Point out each Plasmodium parasite.
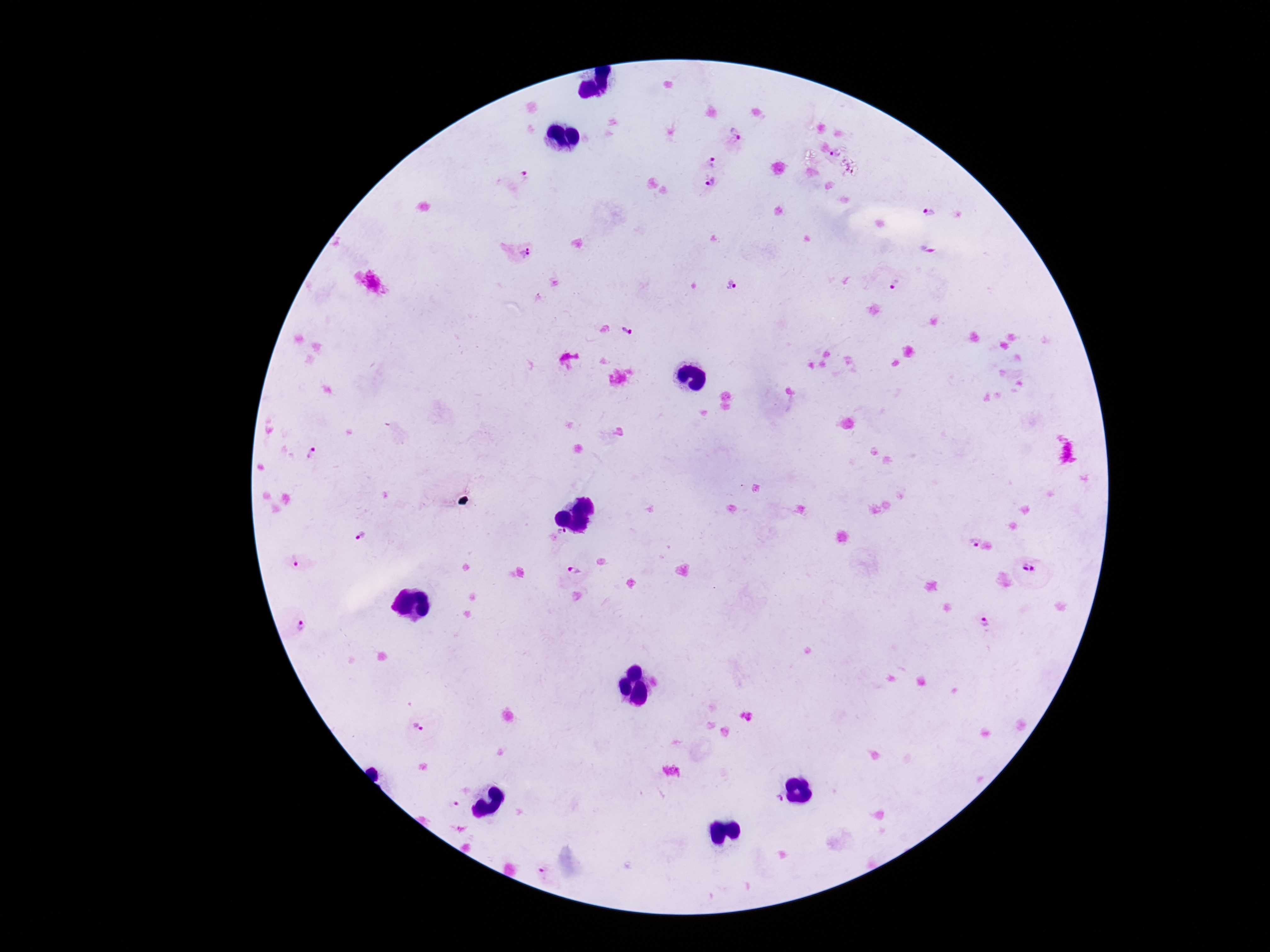

Approximate centers as (x, y) in pixels.
Plasmodium parasites: (736, 131), (834, 151), (711, 161), (520, 176), (711, 184), (928, 210), (514, 252), (889, 284), (733, 287), (626, 329), (312, 455), (561, 537), (361, 539), (974, 544), (300, 561), (574, 571), (1029, 571), (299, 623), (982, 624), (419, 728), (776, 799), (454, 806), (544, 873).

patient malaria status = infected
field of view = single
capture = smartphone camera through the microscope eyepiece
stain = Giemsa
image size = 1270×952 pixels
preparation = thick peripheral-blood smear
magnification = 100x